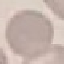
result = negative for malaria parasites
preparation = thin smear
capture = smartphone through the microscope eyepiece
image type = cell patch, automatically extracted from a larger field of view and resized to 64 × 64 pixels
stain = Giemsa